Classify this cell by malaria status.
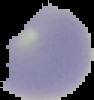
Uninfected.

Image is 94×100 pixels. Cell region segmented out of the field of view; the surrounding area is masked to black. From a thin blood film.